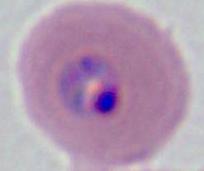
identification: Plasmodium
modality: photomicrograph
magnification: 400x or 1000x